Assess this cell for malaria.
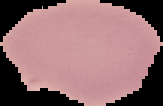

It is uninfected.

image_size: 163×106 pixels
preparation: thin blood film
image_type: segmented cell region with the area outside set to black